Assess for malaria.
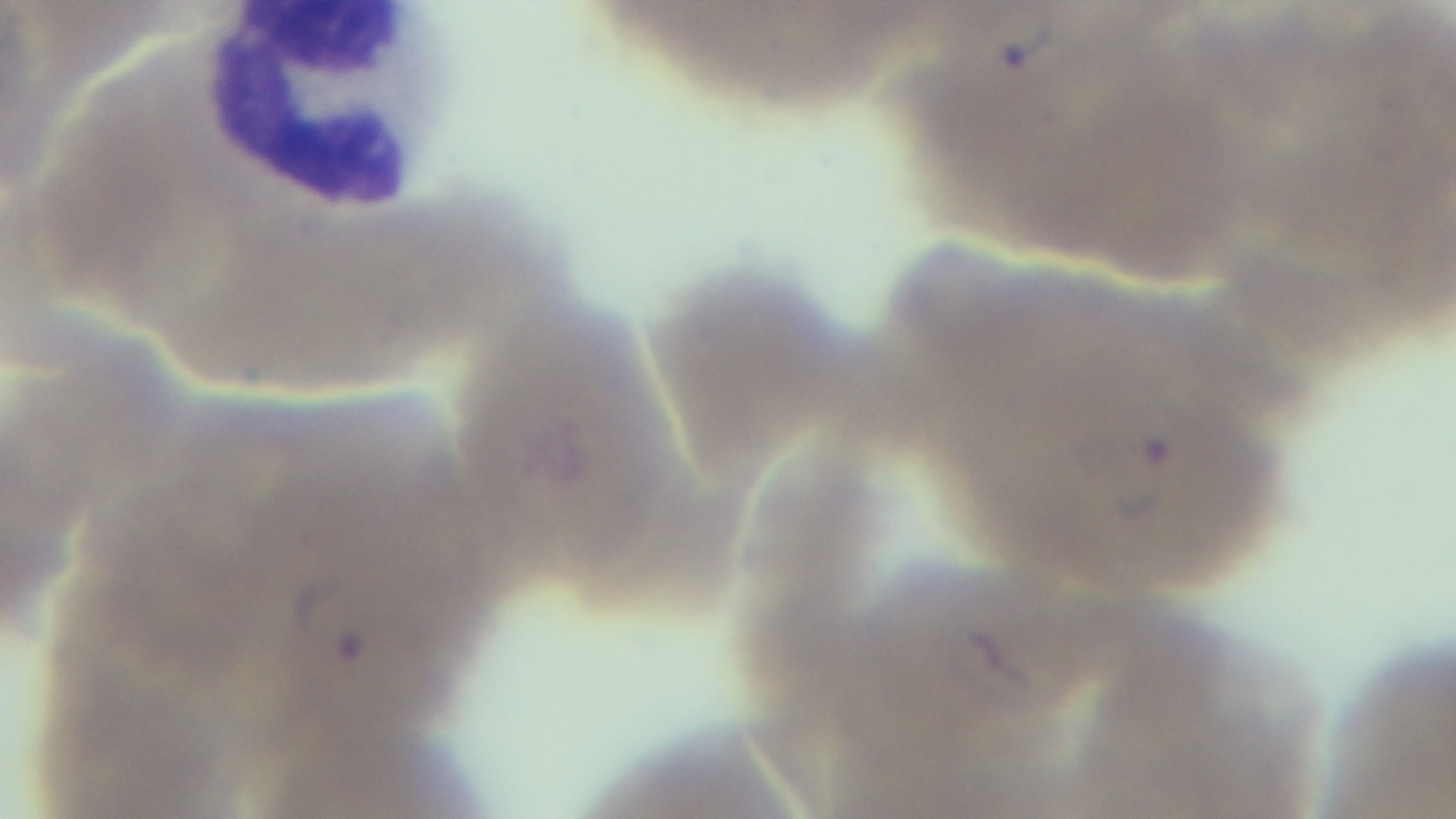

Infected.

Summary:
  - Capture: mounted 4K digital camera
  - Field of view: single
  - Preparation: thin
  - Modality: light microscopy
  - Objective: 100x oil immersion
  - Stain: Giemsa